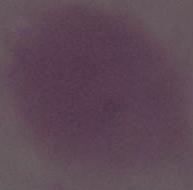
Summary:
  - Magnification: 1000x
  - Modality: photomicrograph
  - Identification: red blood cell